Point out each Plasmodium parasite.
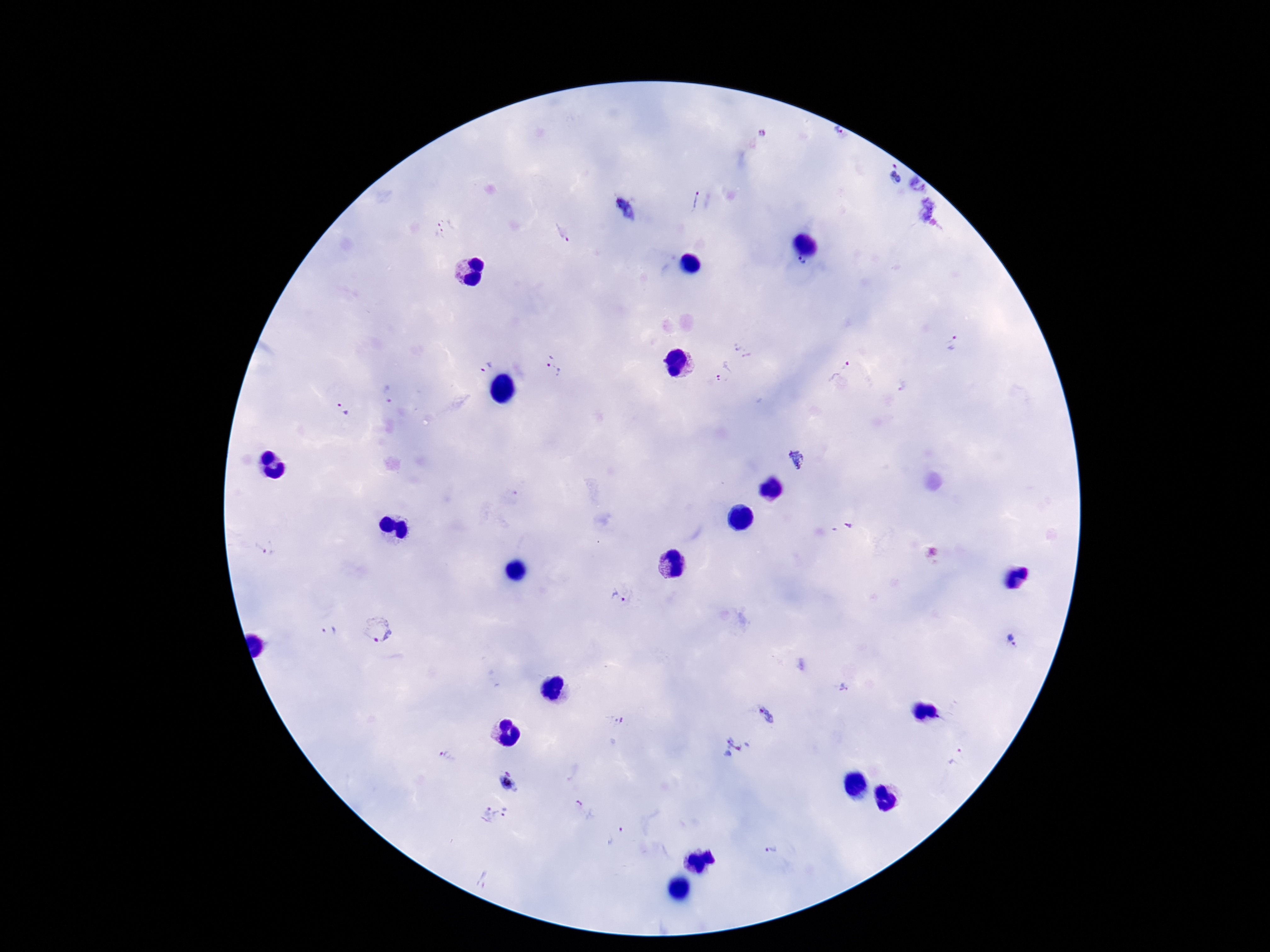

Approximate centers as {x, y} in pixels.
Plasmodium parasites: {837, 131}, {762, 132}, {893, 173}, {917, 184}, {692, 200}, {625, 209}, {927, 211}, {444, 226}, {561, 233}, {802, 263}, {953, 344}, {742, 350}, {482, 364}, {556, 365}, {839, 370}, {722, 371}, {901, 387}, {387, 394}, {342, 411}, {797, 461}, {842, 527}, {264, 548}, {377, 630}, {329, 631}, {1012, 640}, {845, 688}, {766, 716}, {617, 719}, {737, 748}, {956, 756}, {449, 757}, {508, 783}, {579, 803}, {488, 813}, {507, 813}, {621, 829}, {772, 850}, {483, 880}.

Summary:
  - Patient malaria status: infected
  - Magnification: 100x
  - Preparation: thick peripheral-blood smear
  - Image size: 1270×952 pixels
  - Capture: smartphone camera through the microscope eyepiece
  - Field of view: single
  - Stain: Giemsa